Report the malaria status of this cell.
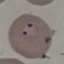

It is parasitized.

preparation = thin blood film
capture = smartphone camera at the microscope eyepiece
image type = automatically extracted cell patch, resized to 64 × 64 pixels
stain = Giemsa